Identify the blood parasite species.
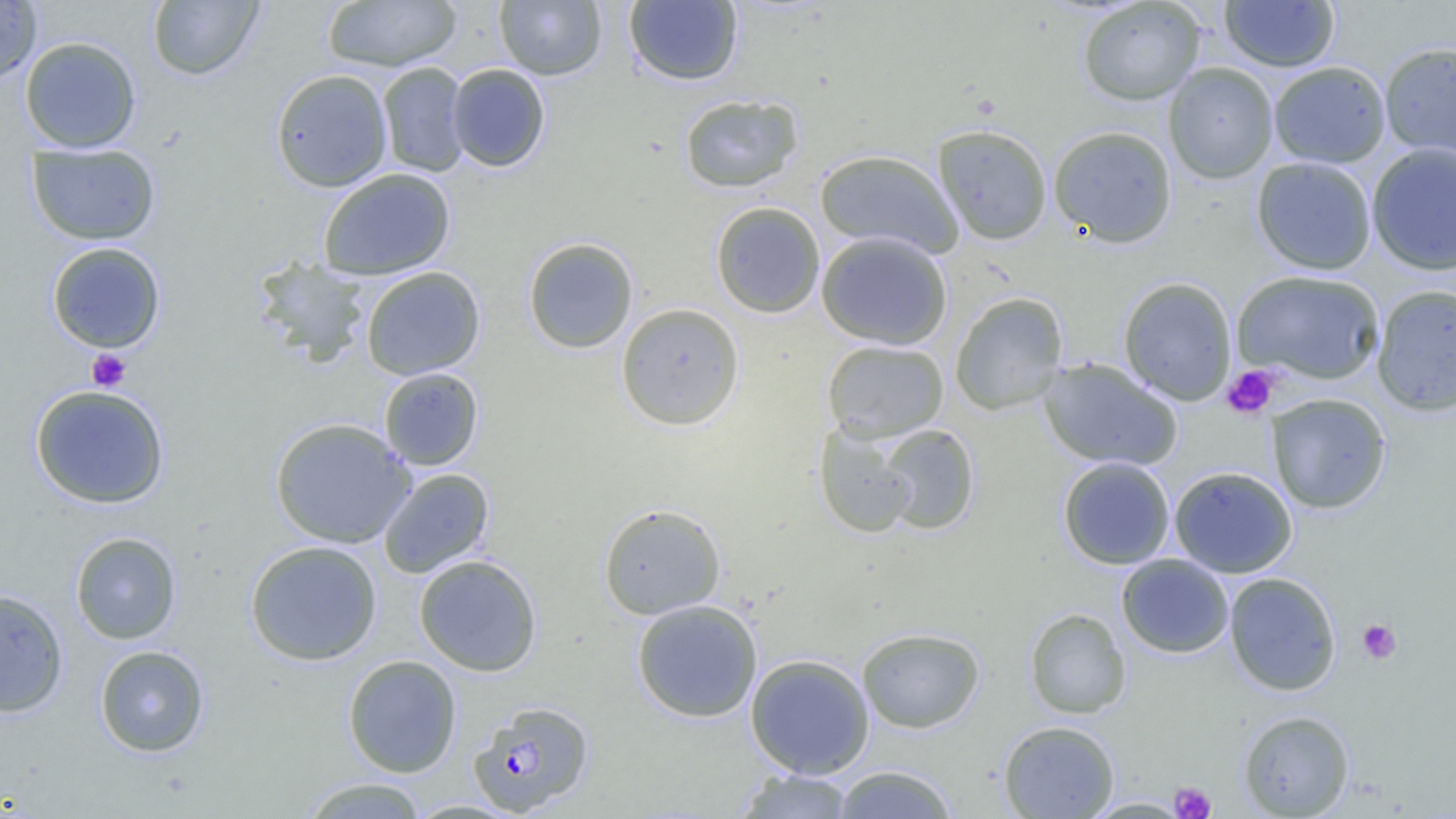

Plasmodium falciparum.

preparation = thin blood film
modality = optical microscopy
platelet locations = approximate bounding boxes as (x1,y1)-(x2,y2) corner pairs in pixels: (86,348)-(131,391), (1222,365)-(1280,418), (1357,619)-(1401,664), (1169,782)-(1216,819)
uninfected red blood cell locations = approximate bounding boxes as (x1,y1)-(x2,y2) corner pairs in pixels: (147,0)-(265,81), (495,0)-(607,80), (1219,0)-(1340,73), (0,1)-(42,86), (322,1)-(462,71), (624,1)-(744,86), (1077,1)-(1207,106), (19,36)-(142,153), (1379,41)-(1456,163), (1268,61)-(1391,168), (377,62)-(471,178), (1163,62)-(1279,184), (446,64)-(551,172), (270,69)-(393,192), (678,93)-(804,193), (933,124)-(1053,245), (1047,125)-(1178,247), (26,143)-(161,245), (1366,143)-(1456,276), (814,148)-(964,259), (1251,156)-(1377,275), (318,167)-(456,281), (710,201)-(825,318), (815,231)-(953,350), (522,236)-(638,354), (46,242)-(166,353), (252,256)-(371,367), (360,266)-(485,380), (1231,270)-(1385,385), (1118,277)-(1237,406), (1371,283)-(1456,416), (949,292)-(1068,416), (616,302)-(745,431), (822,339)-(949,442), (1039,357)-(1182,471), (378,367)-(484,471), (29,384)-(170,509), (1266,393)-(1392,514), (269,417)-(415,549), (814,422)-(921,538), (876,424)-(980,535), (1058,456)-(1175,569), (1169,466)-(1298,578), (378,468)-(495,579), (598,503)-(726,619), (70,531)-(182,644), (245,539)-(383,666), (1116,553)-(1234,659), (414,554)-(542,676), (1224,572)-(1341,696), (0,587)-(69,717), (631,599)-(763,723), (1024,608)-(1131,719), (856,627)-(985,733), (94,645)-(210,757), (745,653)-(875,778), (342,655)-(462,778), (1238,710)-(1355,818), (998,720)-(1119,818), (832,765)-(959,818), (734,769)-(857,818), (299,777)-(430,818)
field of view = single
image size = 1456×819 pixels
magnification = 1000x
Plasmodium falciparum-infected red blood cell locations = approximate bounding boxes as (x1,y1)-(x2,y2) corner pairs in pixels: (469,700)-(595,816)